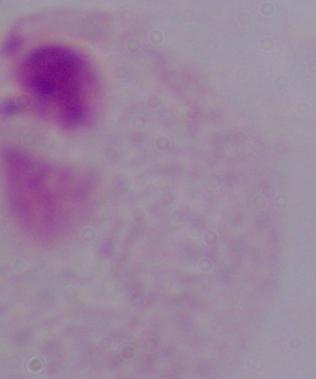
A trichomonad is shown. 1000x magnification. Photomicrograph.